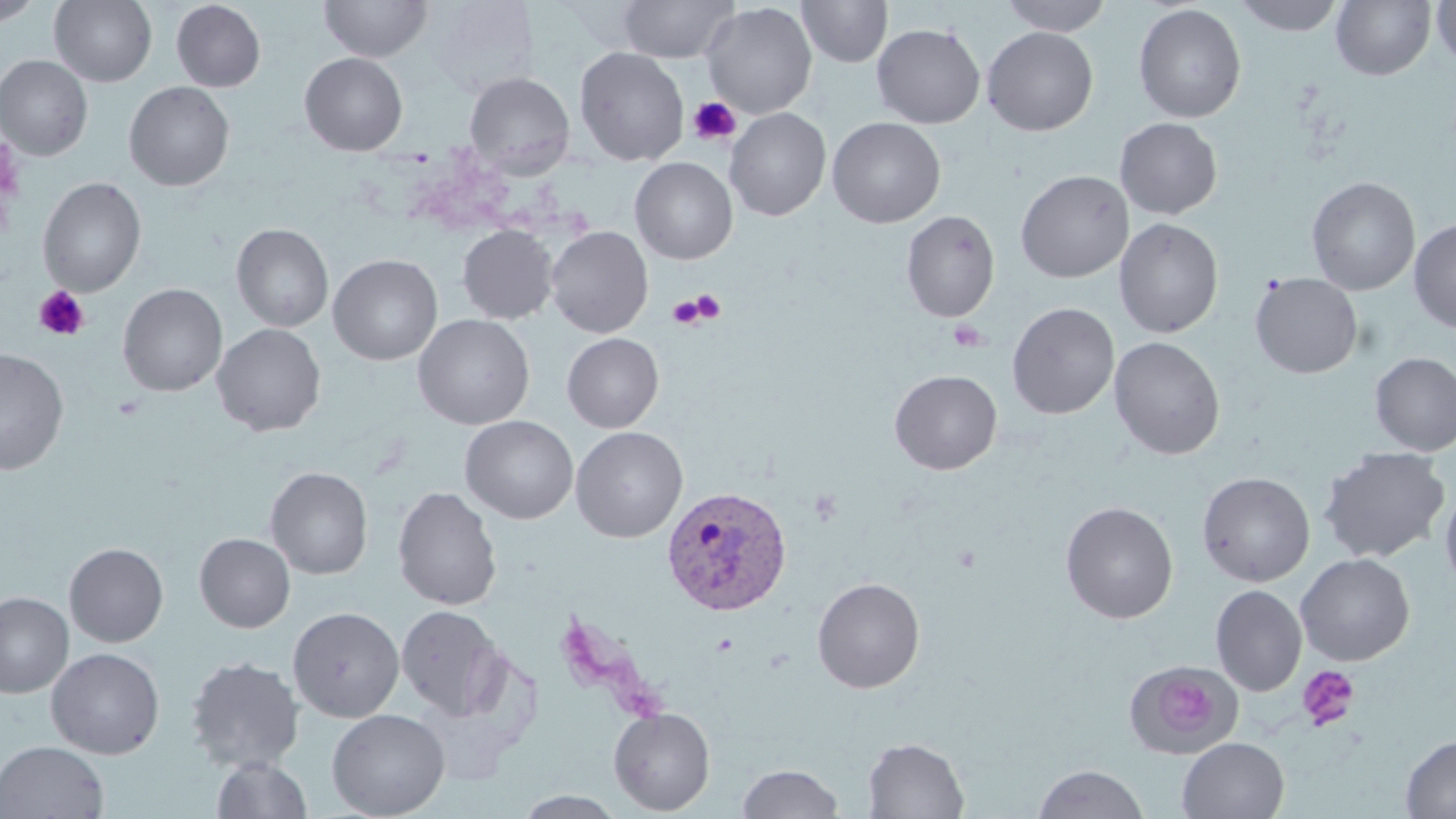

slide-level diagnosis = Plasmodium vivax
platelet locations = approximate bounding boxes as [x1, y1, x2, y2] in pixels: [688, 95, 741, 146], [34, 286, 89, 341], [690, 289, 726, 323], [667, 295, 706, 329], [948, 320, 989, 351], [111, 394, 146, 420], [953, 544, 981, 572], [1297, 665, 1360, 731], [1163, 678, 1212, 732]
preparation = thin blood film
uninfected red blood cell locations = approximate bounding boxes as [x1, y1, x2, y2] in pixels: [0, 0, 44, 27], [50, 0, 157, 87], [320, 0, 432, 62], [618, 0, 738, 63], [998, 0, 1114, 36], [1232, 0, 1345, 36], [171, 1, 266, 92], [425, 1, 539, 97], [796, 1, 893, 68], [1331, 1, 1436, 81], [1431, 1, 1456, 69], [701, 2, 817, 119], [1133, 4, 1247, 123], [872, 23, 986, 128], [982, 26, 1098, 136], [574, 47, 689, 166], [299, 53, 407, 155], [0, 55, 92, 160], [463, 71, 575, 176], [124, 82, 234, 191], [725, 107, 831, 221], [827, 117, 946, 228], [1114, 117, 1223, 219], [630, 157, 738, 264], [1015, 170, 1133, 283], [1306, 176, 1420, 295], [38, 177, 146, 297], [901, 210, 1000, 322], [1114, 217, 1224, 338], [1408, 217, 1456, 333], [232, 224, 333, 332], [457, 225, 557, 324], [546, 226, 653, 338], [328, 254, 443, 365], [1250, 273, 1362, 378], [118, 284, 227, 396], [1007, 302, 1119, 419], [412, 314, 535, 430], [212, 323, 326, 436], [562, 333, 664, 433], [1109, 336, 1225, 460], [0, 349, 69, 476], [1370, 352, 1456, 456], [889, 369, 1002, 475], [461, 416, 578, 524], [571, 426, 688, 542], [1318, 447, 1450, 563], [265, 466, 373, 579], [1197, 471, 1315, 587], [1440, 483, 1456, 593], [393, 486, 502, 610], [1060, 501, 1178, 624], [194, 533, 295, 632], [64, 542, 168, 647], [1296, 553, 1415, 666], [812, 577, 925, 693], [1210, 585, 1307, 695], [0, 591, 74, 698], [397, 604, 504, 720], [287, 607, 405, 722], [46, 647, 165, 759], [185, 655, 304, 772], [1129, 663, 1238, 755], [608, 707, 715, 815], [326, 708, 450, 818], [1401, 734, 1456, 818], [862, 737, 969, 818], [1177, 737, 1290, 819], [0, 741, 109, 819], [211, 756, 313, 818], [738, 764, 844, 819], [1033, 765, 1150, 818], [514, 791, 628, 818]
field of view = single
stain = May-Grünwald-Giemsa
magnification = 1000x
modality = light microscopy
Plasmodium vivax-infected red blood cell locations = approximate bounding boxes as [x1, y1, x2, y2] in pixels: [660, 485, 793, 616]
image size = 1456×819 pixels